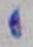

{
  "identification": "Toxoplasma gondii",
  "magnification": "1000x",
  "modality": "photomicrograph"
}